Classify this cell by malaria status.
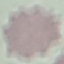
Uninfected.

Giemsa-stained preparation. Thin smear of blood. Acquired by smartphone through the microscope eyepiece. Cell patch, automatically extracted from a larger field of view and resized to 64 × 64 pixels.